Evaluate for Plasmodium parasites.
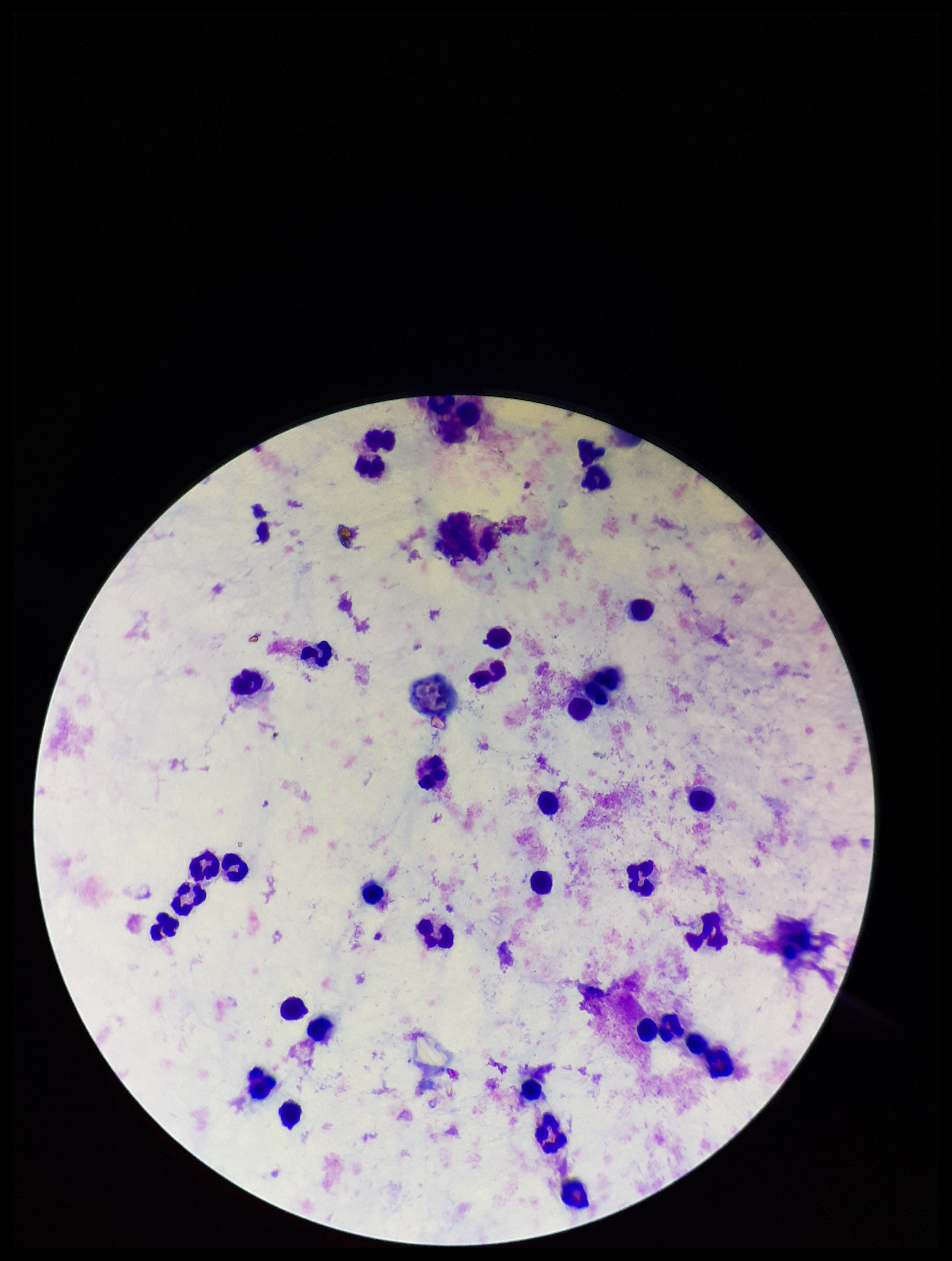
None identified.

Parasite count: 0. Leukocyte count: 35. Photographed through the microscope eyepiece with a smartphone camera. Image is 952×1261 pixels. Patient malaria status: negative. One field from this slide. Stained with Giemsa. Preparation: thick blood smear.